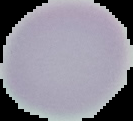

Summary:
  - Image size: 133×121 pixels
  - Preparation: thin blood film
  - Malaria status: uninfected
  - Image type: segmented cell region on a black background